Describe the morphology of the erythrocytes.
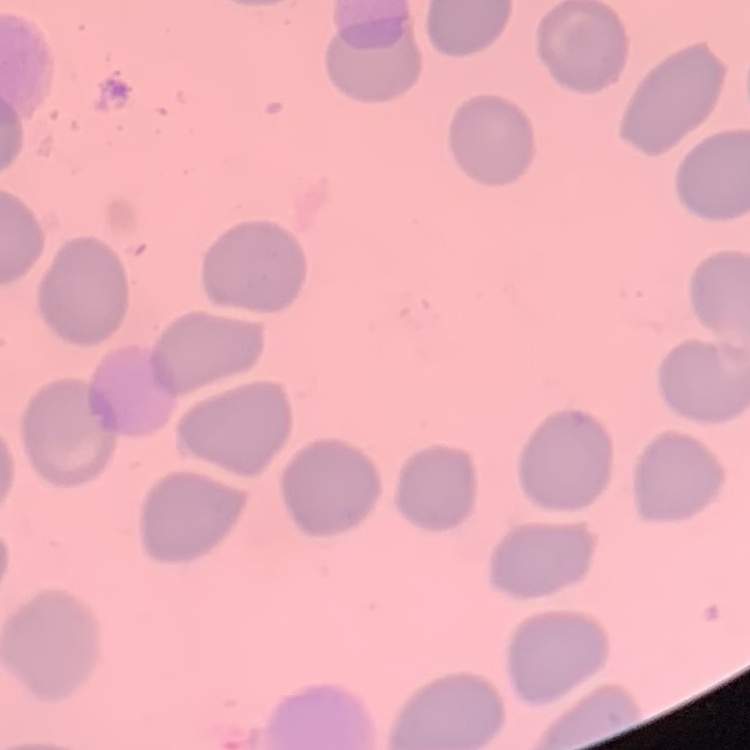
They show no rouleaux formation.

{
  "image_type": "one tile cut from a larger photomicrograph",
  "preparation": "thin peripheral smear",
  "stain": "Field's or Giemsa"
}